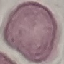

Result: no malaria parasites seen. Giemsa-stained preparation. Thin blood film. Automatically extracted cell patch, resized to 64 × 64 pixels. Acquired by smartphone through the microscope eyepiece.